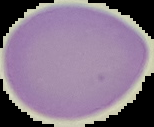
Image is 154×127 pixels. From a thin blood smear. Result: negative for malaria parasites. Cell region segmented out of the field of view; the surrounding area is masked to black.